Classify this cell by malaria status.
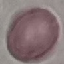

It is uninfected.

Acquired by smartphone through the microscope eyepiece. Thin blood film. Giemsa stain. Cell patch, automatically extracted from a larger field of view and resized to 64 × 64 pixels.